Comment on the morphology of the erythrocytes.
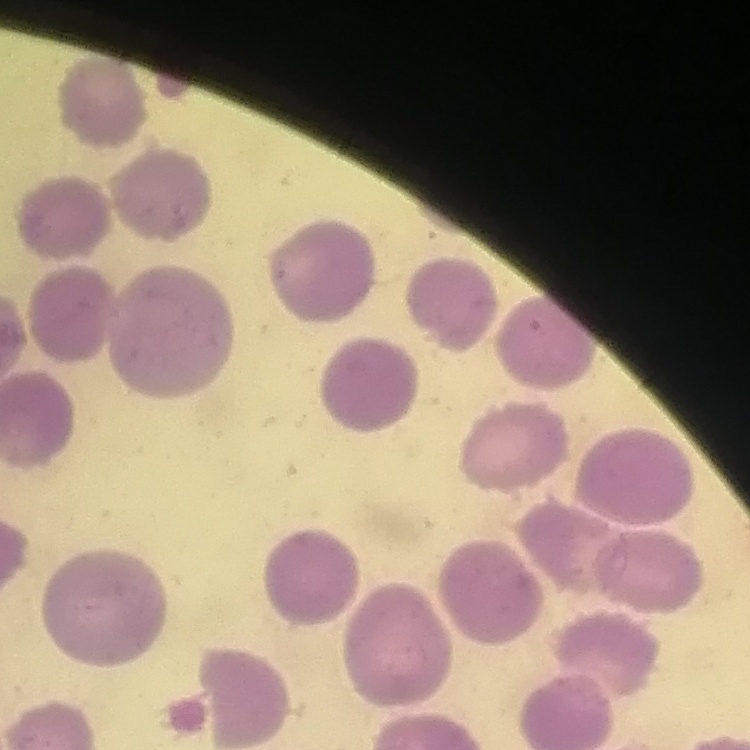

They show no rouleaux formation.

stain = Field's or Giemsa
image type = square crop of a larger photomicrograph
preparation = thin blood smear